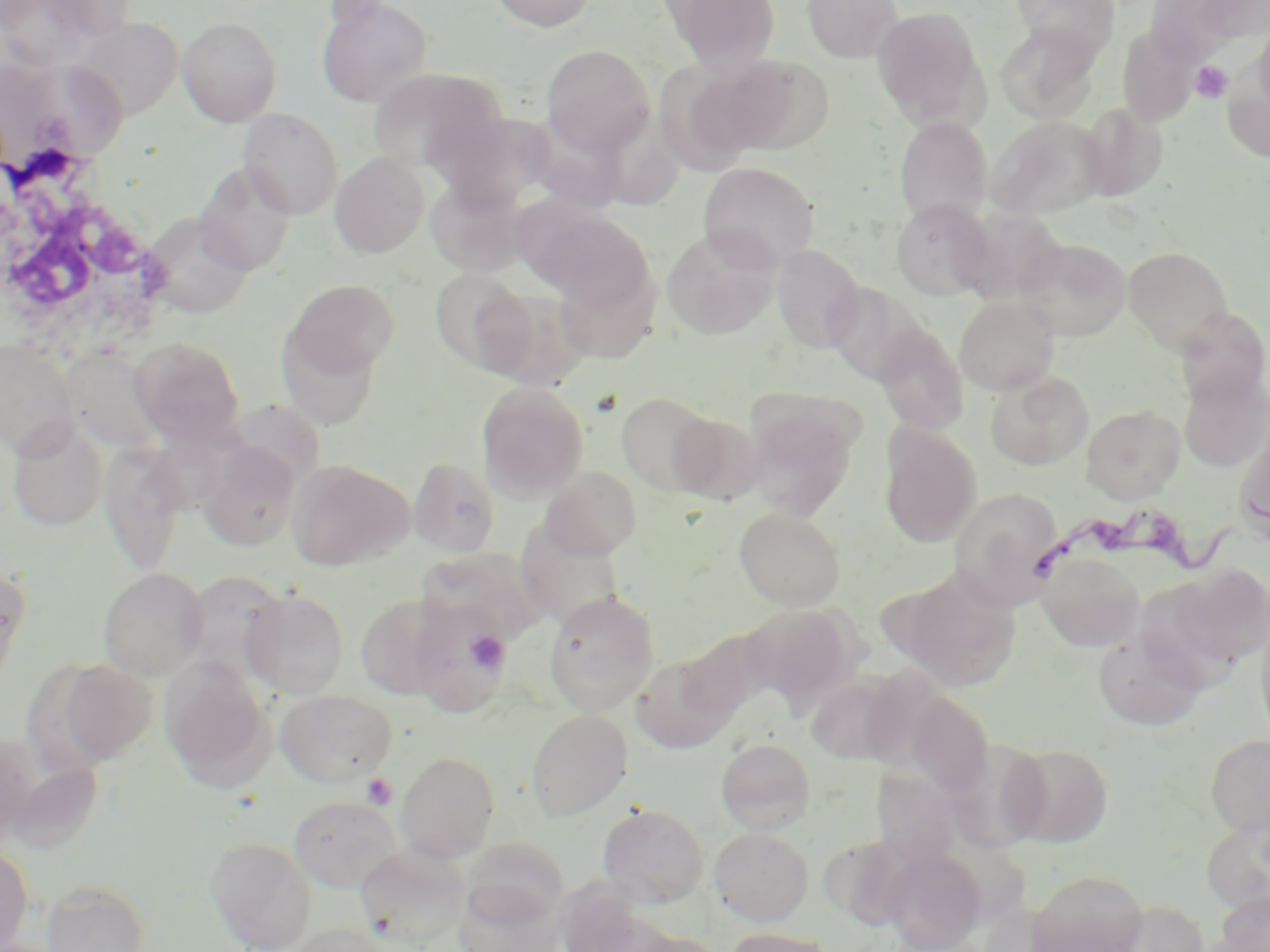

slide-level diagnosis = Trypanosoma brucei
stain = May-Grünwald-Giemsa
field of view = one of a larger specimen
magnification = 1000x
image size = 1270×952 pixels
preparation = thin blood smear
Trypanosoma brucei locations = approximate bounding boxes as (x1,y1)-(x2,y2) corner pairs in pixels: (1031,493)-(1270,587)
platelet locations = approximate bounding boxes as (x1,y1)-(x2,y2) corner pairs in pixels: (1191,61)-(1233,102), (466,628)-(510,674), (362,773)-(398,810)
uninfected red blood cell locations = approximate bounding boxes as (x1,y1)-(x2,y2) corner pairs in pixels: (0,0)-(105,68), (315,0)-(432,108), (487,0)-(598,32), (658,0)-(781,73), (803,0)-(902,63), (1011,1)-(1120,61), (1193,1)-(1270,43), (1146,2)-(1250,61), (871,7)-(988,129), (178,16)-(282,126), (71,17)-(183,121), (1253,18)-(1270,121), (995,23)-(1100,122), (1117,27)-(1199,127), (541,44)-(655,157), (708,53)-(834,156), (654,57)-(777,174), (1222,66)-(1270,163), (36,69)-(134,160), (1077,102)-(1168,202), (603,104)-(690,210), (521,107)-(640,207), (239,108)-(343,219), (442,111)-(560,210), (986,116)-(1108,220), (894,117)-(993,225), (330,152)-(429,258), (194,162)-(297,275), (698,162)-(819,270), (426,178)-(527,277), (891,199)-(996,301), (528,206)-(655,312), (144,213)-(252,317), (968,213)-(1079,309), (661,228)-(781,339), (1015,237)-(1131,341), (772,245)-(865,352), (1124,247)-(1233,352), (552,262)-(660,364), (430,269)-(533,372), (284,278)-(399,383), (824,281)-(931,386), (955,296)-(1059,395), (1172,307)-(1269,406), (277,322)-(384,430), (874,324)-(968,434), (129,338)-(245,446), (0,341)-(79,458), (63,347)-(165,454), (1178,370)-(1270,472), (985,371)-(1094,470), (477,382)-(589,502), (615,391)-(718,495), (744,393)-(862,520), (1081,404)-(1185,504), (667,411)-(761,503), (8,419)-(108,532), (878,423)-(982,547), (1235,429)-(1270,542), (101,441)-(189,575), (197,442)-(301,551), (408,457)-(500,557), (288,460)-(414,571), (539,466)-(643,560), (950,487)-(1064,608), (734,507)-(846,610), (516,522)-(626,630), (415,547)-(548,647), (1037,551)-(1145,651), (0,564)-(30,695), (1176,566)-(1269,667), (98,567)-(209,679), (179,568)-(290,686), (894,568)-(1021,691), (242,588)-(349,699), (543,590)-(659,715), (355,594)-(452,701), (408,602)-(512,717), (744,603)-(858,707), (1255,615)-(1270,747), (676,629)-(772,726), (1093,630)-(1206,731), (632,652)-(739,753), (160,658)-(275,790), (55,659)-(157,765), (806,670)-(910,765), (275,689)-(397,786), (904,692)-(995,794), (526,709)-(632,822), (1204,733)-(1270,835), (0,734)-(40,843), (716,738)-(816,834), (1004,743)-(1114,847), (396,751)-(500,862), (8,758)-(103,853), (881,766)-(965,875), (288,795)-(404,894), (597,803)-(709,908), (1201,817)-(1270,916), (709,827)-(813,926), (820,833)-(919,929), (206,836)-(317,951), (460,836)-(570,927), (355,844)-(472,950), (0,845)-(33,952), (881,849)-(987,952), (1026,870)-(1150,952), (41,879)-(149,952), (454,882)-(564,952), (1213,888)-(1270,952), (1104,900)-(1210,952), (286,923)-(395,952), (721,927)-(842,952), (623,929)-(723,952)
white blood cell locations = approximate bounding boxes as (x1,y1)-(x2,y2) corner pairs in pixels: (0,163)-(173,359)
modality = light microscopy